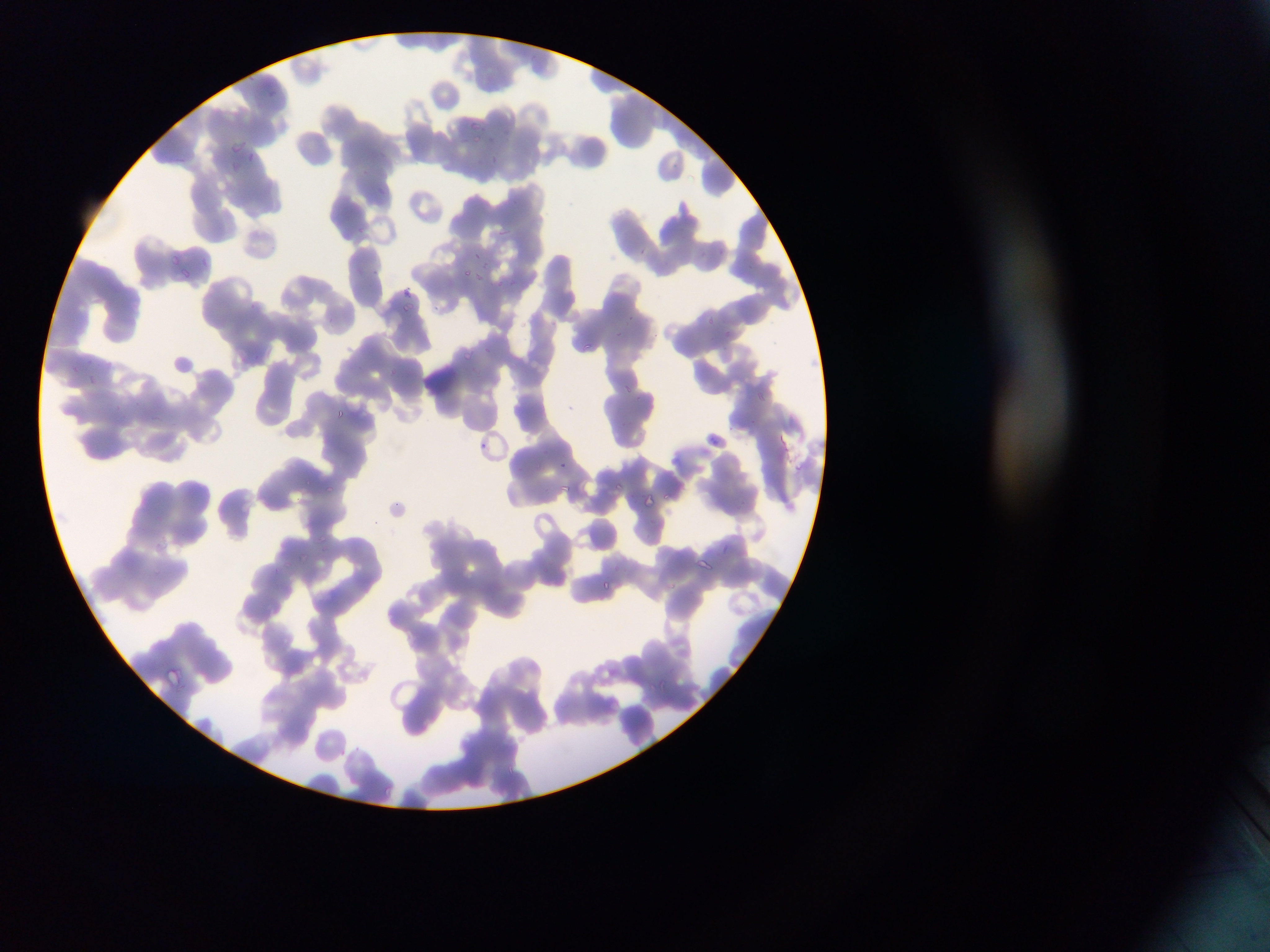
Approximate bounding boxes as {left, top, right, bottom} in pixels.
Summary:
  - Plasmodium parasite locations: {267, 84, 279, 100}, {472, 118, 479, 130}, {464, 134, 485, 148}, {229, 138, 243, 147}, {248, 149, 256, 161}, {488, 154, 499, 173}, {226, 161, 243, 173}, {376, 181, 396, 198}, {498, 223, 521, 249}, {640, 243, 656, 263}, {715, 245, 728, 257}, {468, 248, 490, 266}, {167, 252, 181, 269}, {476, 265, 483, 280}, {463, 268, 474, 285}, {172, 271, 189, 283}, {496, 277, 511, 293}, {400, 284, 413, 296}, {401, 303, 418, 314}, {703, 311, 718, 331}, {726, 327, 733, 340}, {574, 339, 593, 355}, {463, 349, 488, 374}, {174, 350, 199, 373}, {70, 364, 87, 381}, {626, 382, 639, 405}, {756, 385, 773, 411}, {336, 409, 348, 420}, {706, 433, 718, 447}, {479, 440, 489, 454}, {559, 459, 571, 470}, {614, 479, 636, 496}, {316, 481, 333, 496}, {560, 483, 575, 501}, {662, 492, 674, 505}, {644, 494, 664, 524}, {389, 497, 412, 514}, {154, 532, 172, 552}, {317, 541, 340, 556}, {693, 554, 724, 580}, {277, 577, 293, 588}, {601, 579, 622, 598}, {163, 667, 180, 688}
  - Country: Ghana
  - Preparation: thin blood smear
  - Image size: 1270×952 pixels
  - Field of view: single
  - Capture: mobile-phone photograph through a microscope